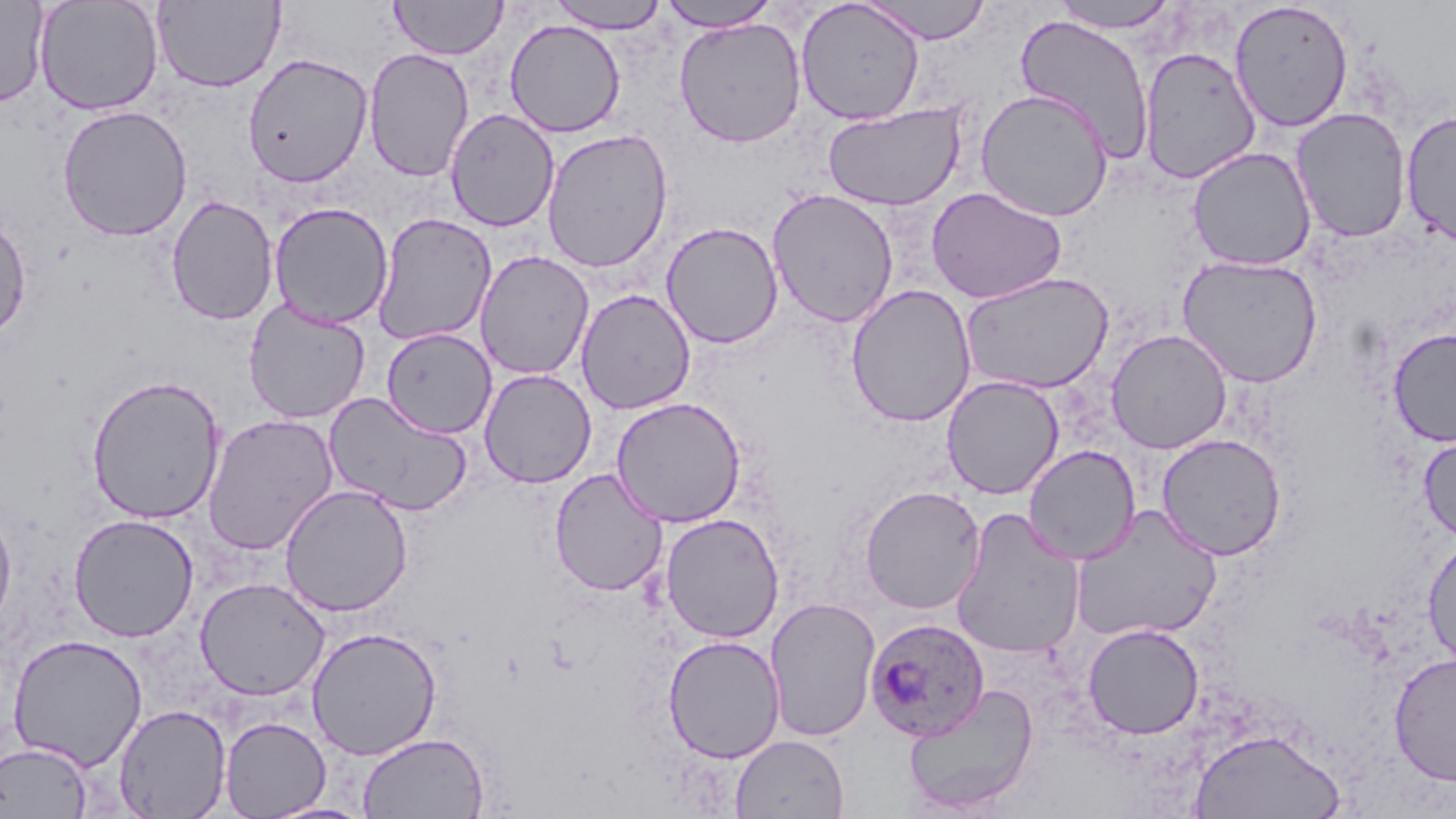
slide-level diagnosis = Plasmodium ovale
magnification = 1000x
image size = 1456×819 pixels
uninfected red blood cell locations = approximate bounding boxes as (x1, y1, x2, y2) in pixels: (0, 0, 50, 107), (34, 0, 164, 116), (390, 0, 508, 60), (548, 0, 670, 33), (860, 0, 994, 44), (152, 1, 285, 92), (658, 1, 782, 32), (795, 1, 925, 125), (1050, 1, 1181, 33), (1229, 1, 1354, 133), (1014, 14, 1156, 165), (674, 17, 807, 148), (504, 19, 626, 138), (1138, 46, 1261, 184), (363, 47, 474, 182), (242, 52, 373, 188), (975, 88, 1113, 222), (822, 102, 968, 211), (57, 104, 193, 241), (1291, 107, 1412, 243), (445, 108, 560, 232), (1400, 109, 1456, 247), (541, 128, 674, 274), (1187, 146, 1316, 270), (926, 186, 1068, 304), (766, 189, 900, 328), (165, 195, 279, 326), (268, 202, 393, 329), (0, 213, 32, 344), (372, 213, 497, 346), (661, 222, 784, 348), (475, 250, 594, 381), (1177, 255, 1324, 388), (959, 271, 1114, 395), (846, 284, 977, 428), (576, 289, 696, 414), (243, 299, 371, 424), (381, 327, 497, 438), (1387, 328, 1456, 446), (1105, 329, 1232, 454), (478, 369, 597, 488), (86, 374, 226, 524), (941, 375, 1064, 499), (323, 391, 475, 516), (610, 396, 747, 528), (202, 413, 339, 556), (1155, 433, 1288, 560), (1417, 433, 1456, 543), (1023, 445, 1141, 565), (549, 468, 668, 597), (279, 484, 413, 617), (859, 485, 986, 614), (0, 501, 17, 635), (1071, 505, 1222, 643), (951, 507, 1085, 659), (67, 513, 199, 642), (660, 513, 784, 642), (1422, 533, 1456, 670), (195, 577, 330, 701), (764, 596, 881, 742), (1083, 623, 1205, 740), (306, 626, 442, 760), (7, 633, 148, 771), (662, 635, 785, 762), (1389, 652, 1456, 785), (904, 684, 1039, 815), (113, 703, 232, 818), (219, 716, 331, 818), (1188, 728, 1346, 818), (357, 732, 490, 818), (730, 734, 850, 818), (0, 740, 94, 818), (261, 800, 376, 819)
Plasmodium ovale-infected red blood cell locations = approximate bounding boxes as (x1, y1, x2, y2) in pixels: (865, 617, 989, 741)
field of view = one of a larger specimen
preparation = thin blood smear
stain = May-Grünwald-Giemsa
modality = optical microscopy